Locate and identify every blood parasite.
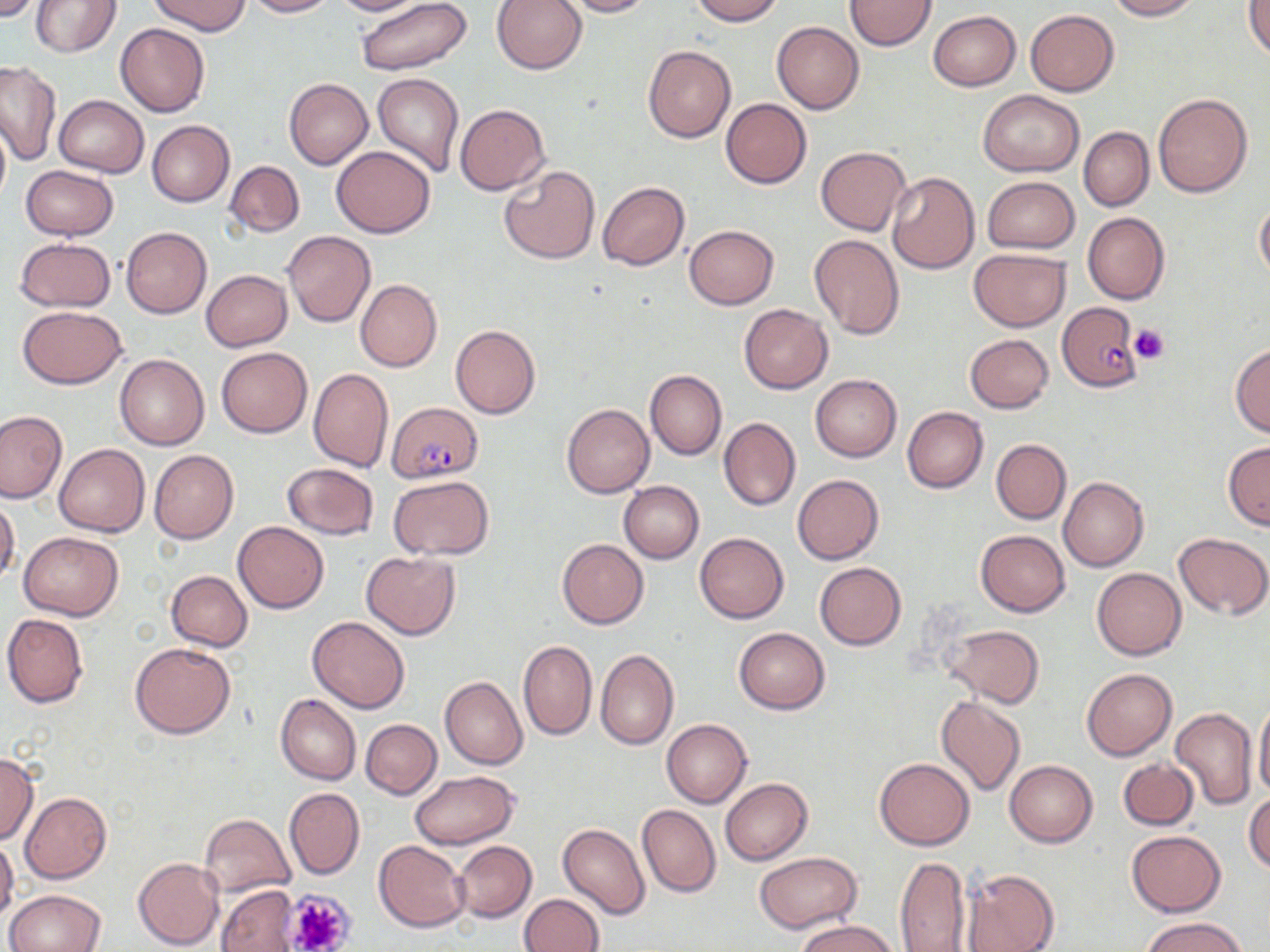

Approximate bounding boxes as (x1,y1)-(x2,y2) corner pairs in pixels.
Plasmodium falciparum-infected red blood cells: (1057,303)-(1143,390), (387,402)-(483,483).
No Plasmodium ovale, Plasmodium malariae, Plasmodium vivax, Babesia divergens, or Trypanosoma brucei observed.

Uninfected red blood cell locations: (0,0)-(46,21), (150,0)-(250,36), (243,0)-(334,17), (329,0)-(422,15), (356,0)-(473,75), (560,0)-(654,17), (689,0)-(782,24), (845,0)-(935,50), (1103,0)-(1200,20), (31,1)-(121,57), (491,1)-(586,74), (1245,1)-(1270,61), (1026,9)-(1120,96), (928,10)-(1021,91), (773,22)-(864,115), (116,23)-(210,117), (643,45)-(736,142), (0,61)-(60,163), (372,74)-(464,178), (284,78)-(373,169), (978,89)-(1084,176), (1152,93)-(1253,197), (54,94)-(149,177), (720,99)-(811,188), (455,104)-(549,194), (0,114)-(10,209), (148,120)-(234,207), (1079,127)-(1153,211), (331,144)-(435,238), (816,146)-(911,236), (224,160)-(305,238), (499,165)-(600,264), (20,166)-(118,239), (887,171)-(979,273), (982,176)-(1079,254), (597,182)-(690,271), (1254,200)-(1270,281), (1083,212)-(1169,304), (685,224)-(778,309), (120,227)-(212,318), (281,231)-(375,327), (809,233)-(905,340), (15,237)-(115,312), (968,248)-(1071,331), (201,270)-(293,351), (355,279)-(443,372), (738,303)-(833,394), (17,305)-(128,387), (450,325)-(541,418), (964,334)-(1055,413), (1230,343)-(1270,437), (216,347)-(312,437), (115,354)-(209,450), (309,367)-(394,472), (645,370)-(727,459), (810,374)-(902,461), (561,402)-(654,497), (902,406)-(989,493), (0,411)-(66,503), (718,417)-(800,511), (991,439)-(1070,524), (1223,440)-(1270,530), (54,444)-(149,537), (149,450)-(238,543), (281,463)-(379,540), (793,474)-(884,565), (387,475)-(494,560), (1059,477)-(1149,571), (619,481)-(704,563), (0,497)-(20,585), (232,521)-(329,613), (18,530)-(123,620), (975,530)-(1070,617), (695,532)-(789,623), (1174,532)-(1270,619), (557,537)-(649,628), (360,552)-(460,640), (814,562)-(906,650), (1092,567)-(1186,660), (167,570)-(253,651), (2,614)-(89,708), (306,616)-(409,713), (942,624)-(1045,707), (734,627)-(829,714), (520,640)-(598,740), (130,642)-(235,739), (596,649)-(679,749), (1082,668)-(1177,760), (440,677)-(527,769), (276,694)-(361,785), (936,695)-(1026,798), (1253,700)-(1270,800), (1170,705)-(1257,810), (661,718)-(752,808), (360,719)-(441,799), (0,753)-(39,845), (1119,757)-(1199,830), (875,758)-(974,850), (1005,760)-(1097,847), (409,770)-(519,849), (721,778)-(812,865), (283,787)-(365,880), (21,792)-(112,883), (1244,794)-(1270,873), (637,804)-(720,898), (199,814)-(295,899), (558,823)-(650,919), (1127,830)-(1225,915), (0,837)-(19,923), (373,841)-(470,931), (453,842)-(535,923), (754,851)-(864,933), (893,854)-(970,951), (133,856)-(224,950), (961,868)-(1060,952), (217,884)-(300,952), (5,889)-(106,952), (520,893)-(604,952), (1142,917)-(1249,952), (794,918)-(902,952). Platelet locations: (1130,324)-(1169,364), (284,889)-(356,952). Slide-level diagnosis: Plasmodium falciparum. Image is 1270×952 pixels. Thin blood smear. Captured at 1000x magnification. Single field of view. May-Grünwald-Giemsa stain. Optical microscopy.